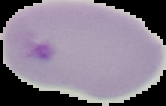

Segmented cell region on a black background. Image is 166×106 pixels. From a thin blood film. Result: no malaria parasites seen.